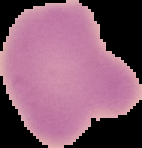
image type = segmented cell region on a black background
image size = 142×148 pixels
malaria status = uninfected
preparation = thin blood smear